State which parasite is depicted.
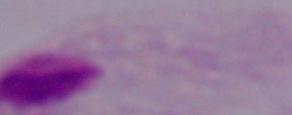
This is a trichomonad.

Summary:
  - Magnification: 1000x
  - Modality: photomicrograph